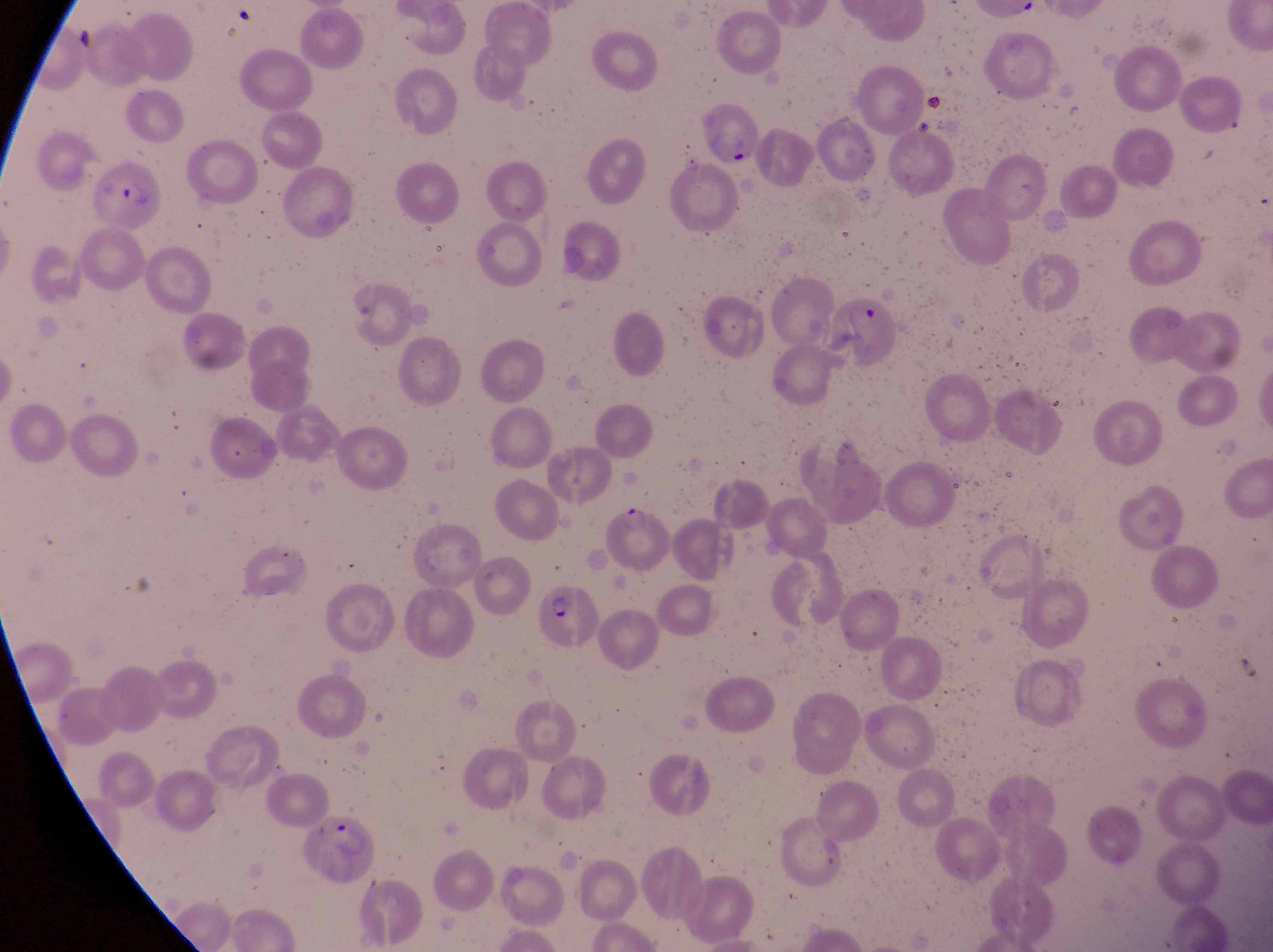

Approximate bounding boxes as {left, top, right, bottom} in pixels. Parasitised red blood cell locations: {697, 100, 762, 167}, {90, 158, 167, 232}, {826, 295, 900, 370}, {607, 504, 672, 569}, {537, 587, 599, 645}, {294, 819, 379, 887}. Artifact (platelet-like body, stain precipitate, or debris) locations: {232, 8, 260, 26}, {63, 18, 103, 66}, {917, 87, 947, 120}. Single field of view. Image is 1273×952 pixels. At a magnification of 1000x. Thin blood smear. Sample from Uganda. Photographed through the eyepiece of an Olympus CX-23 microscope with a smartphone camera.